Assess this cell for malaria.
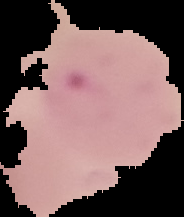
It is parasitized.

image_size: 184×217 pixels
image_type: cell region segmented out of the field of view; surrounding area masked to black
preparation: thin blood film